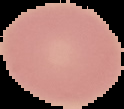 From a thin blood smear. Cell region segmented out of the field of view; the surrounding area is masked to black. Result: negative for Plasmodium parasites. Image is 124×109 pixels.